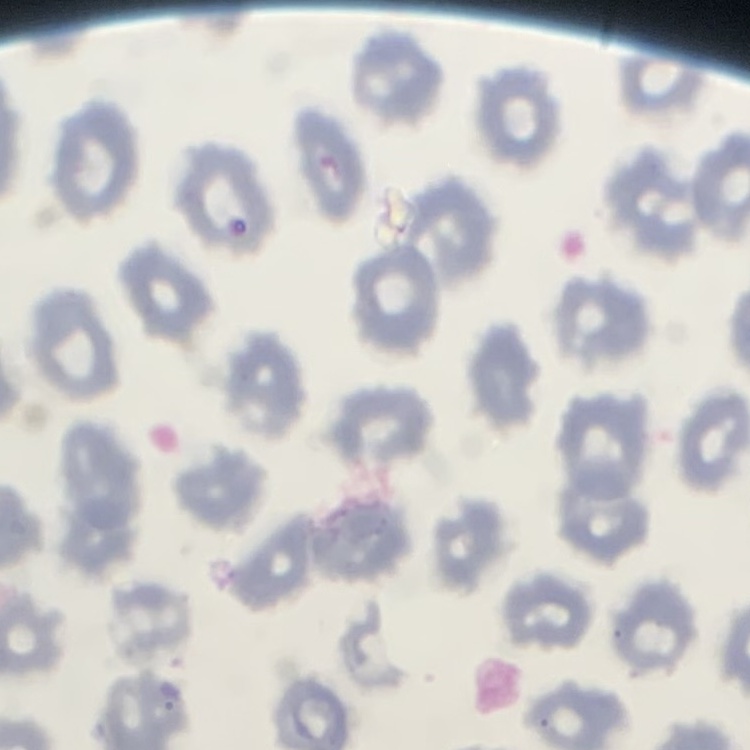

red blood cell morphology = no rouleaux formation
image type = one tile cut from a larger photomicrograph
stain = Field's or Giemsa
preparation = thin blood smear